Name the parasite shown.
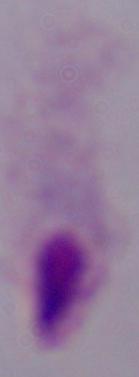
A trichomonad.

modality = photomicrograph
magnification = 1000x